Locate and identify every blood parasite.
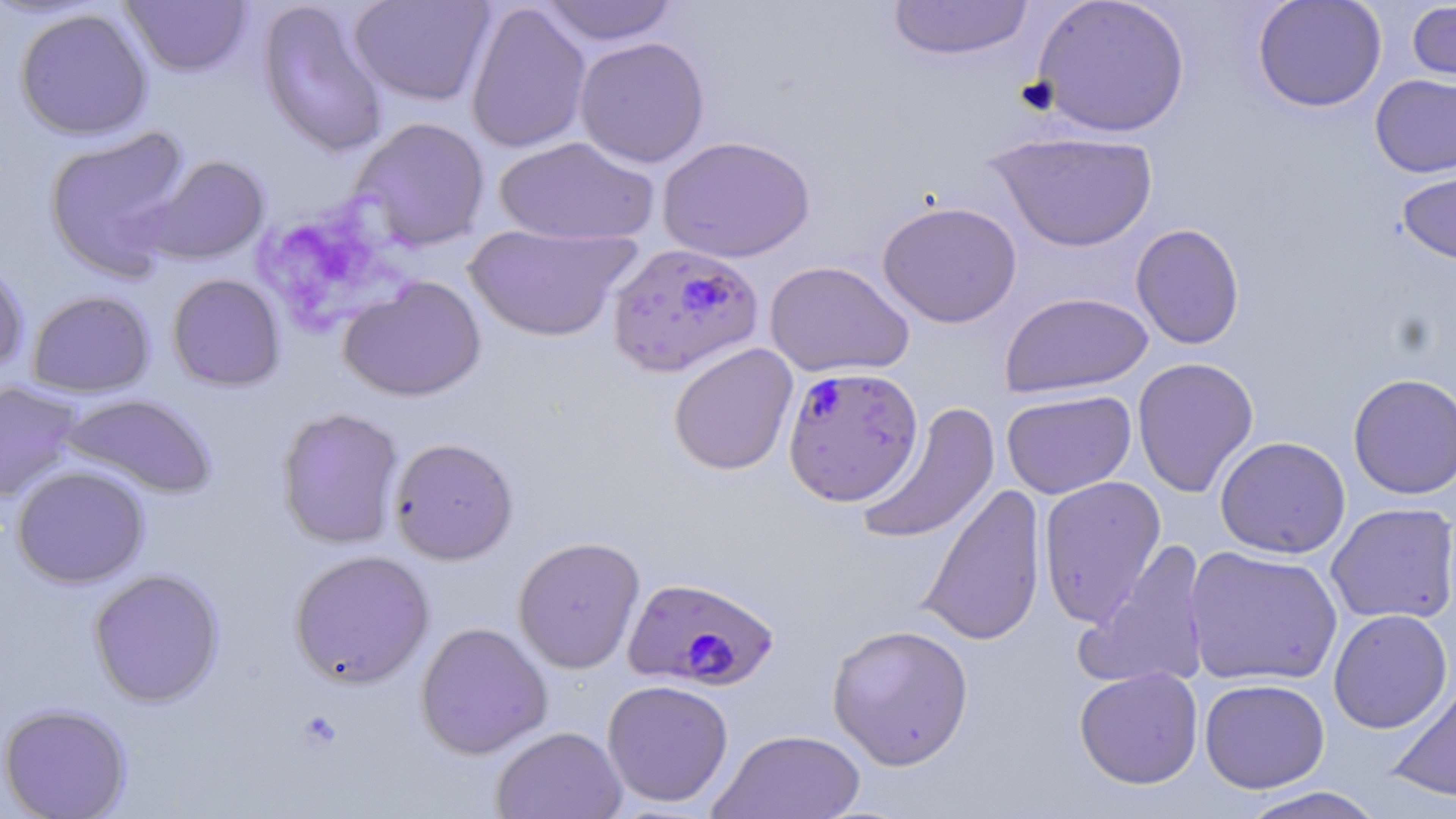

Approximate bounding boxes as named x1/y1/x2/y2 corners in pixels.
Plasmodium falciparum-infected red blood cells: (x1=606, y1=242, x2=764, y2=378), (x1=782, y1=365, x2=923, y2=505), (x1=623, y1=575, x2=780, y2=691).
No Plasmodium ovale, Plasmodium malariae, Plasmodium vivax, Babesia divergens, or Trypanosoma brucei observed.

Summary:
  - Uninfected red blood cell locations: (x1=257, y1=0, x2=391, y2=158), (x1=348, y1=0, x2=495, y2=107), (x1=886, y1=0, x2=1034, y2=62), (x1=1030, y1=0, x2=1191, y2=138), (x1=1251, y1=0, x2=1387, y2=113), (x1=120, y1=1, x2=252, y2=77), (x1=538, y1=1, x2=679, y2=46), (x1=1406, y1=1, x2=1456, y2=87), (x1=465, y1=2, x2=592, y2=154), (x1=14, y1=8, x2=153, y2=141), (x1=574, y1=36, x2=710, y2=168), (x1=1369, y1=74, x2=1456, y2=178), (x1=351, y1=117, x2=491, y2=251), (x1=43, y1=126, x2=194, y2=281), (x1=987, y1=130, x2=1159, y2=253), (x1=657, y1=134, x2=816, y2=263), (x1=493, y1=135, x2=659, y2=246), (x1=143, y1=155, x2=270, y2=266), (x1=1396, y1=163, x2=1456, y2=267), (x1=877, y1=199, x2=1022, y2=328), (x1=1131, y1=223, x2=1245, y2=350), (x1=464, y1=224, x2=641, y2=342), (x1=0, y1=255, x2=30, y2=376), (x1=764, y1=260, x2=914, y2=378), (x1=167, y1=273, x2=286, y2=392), (x1=338, y1=276, x2=487, y2=402), (x1=27, y1=290, x2=155, y2=398), (x1=1000, y1=291, x2=1153, y2=398), (x1=668, y1=343, x2=798, y2=476), (x1=1132, y1=357, x2=1259, y2=498), (x1=1347, y1=372, x2=1456, y2=500), (x1=0, y1=380, x2=84, y2=503), (x1=1001, y1=389, x2=1137, y2=499), (x1=57, y1=393, x2=218, y2=499), (x1=856, y1=402, x2=1000, y2=547), (x1=276, y1=407, x2=404, y2=550), (x1=388, y1=436, x2=519, y2=565), (x1=1214, y1=436, x2=1351, y2=559), (x1=11, y1=465, x2=150, y2=588), (x1=1038, y1=476, x2=1167, y2=627), (x1=918, y1=482, x2=1047, y2=646), (x1=1326, y1=502, x2=1456, y2=625), (x1=512, y1=535, x2=646, y2=674), (x1=1075, y1=540, x2=1212, y2=691), (x1=1184, y1=546, x2=1343, y2=687), (x1=288, y1=549, x2=434, y2=689), (x1=88, y1=568, x2=225, y2=707), (x1=1328, y1=609, x2=1453, y2=734), (x1=415, y1=621, x2=553, y2=760), (x1=827, y1=623, x2=975, y2=770), (x1=1074, y1=667, x2=1204, y2=789), (x1=1198, y1=678, x2=1330, y2=793), (x1=602, y1=679, x2=734, y2=807), (x1=1387, y1=680, x2=1456, y2=803), (x1=0, y1=702, x2=132, y2=819), (x1=491, y1=725, x2=628, y2=819), (x1=709, y1=728, x2=867, y2=819), (x1=1235, y1=786, x2=1389, y2=819)
  - Platelet locations: (x1=263, y1=191, x2=434, y2=328), (x1=295, y1=712, x2=342, y2=753)
  - Slide-level diagnosis: Plasmodium falciparum
  - Magnification: 1000x
  - Stain: May-Grünwald-Giemsa
  - Field of view: single
  - Image size: 1456×819 pixels
  - Preparation: thin blood smear
  - Modality: optical microscopy